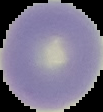

{
  "preparation": "thin blood smear",
  "image_type": "cell region segmented out of the field of view; surrounding area masked to black",
  "image_size": "103×112 pixels",
  "result": "negative for malaria parasites"
}